Identify the parasite.
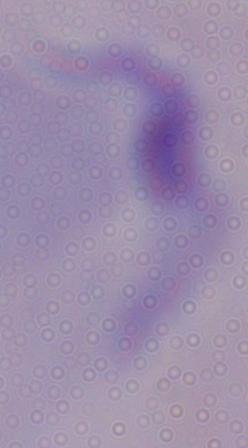
This is a trypanosome.

Summary:
  - Magnification: 1000x
  - Modality: micrograph